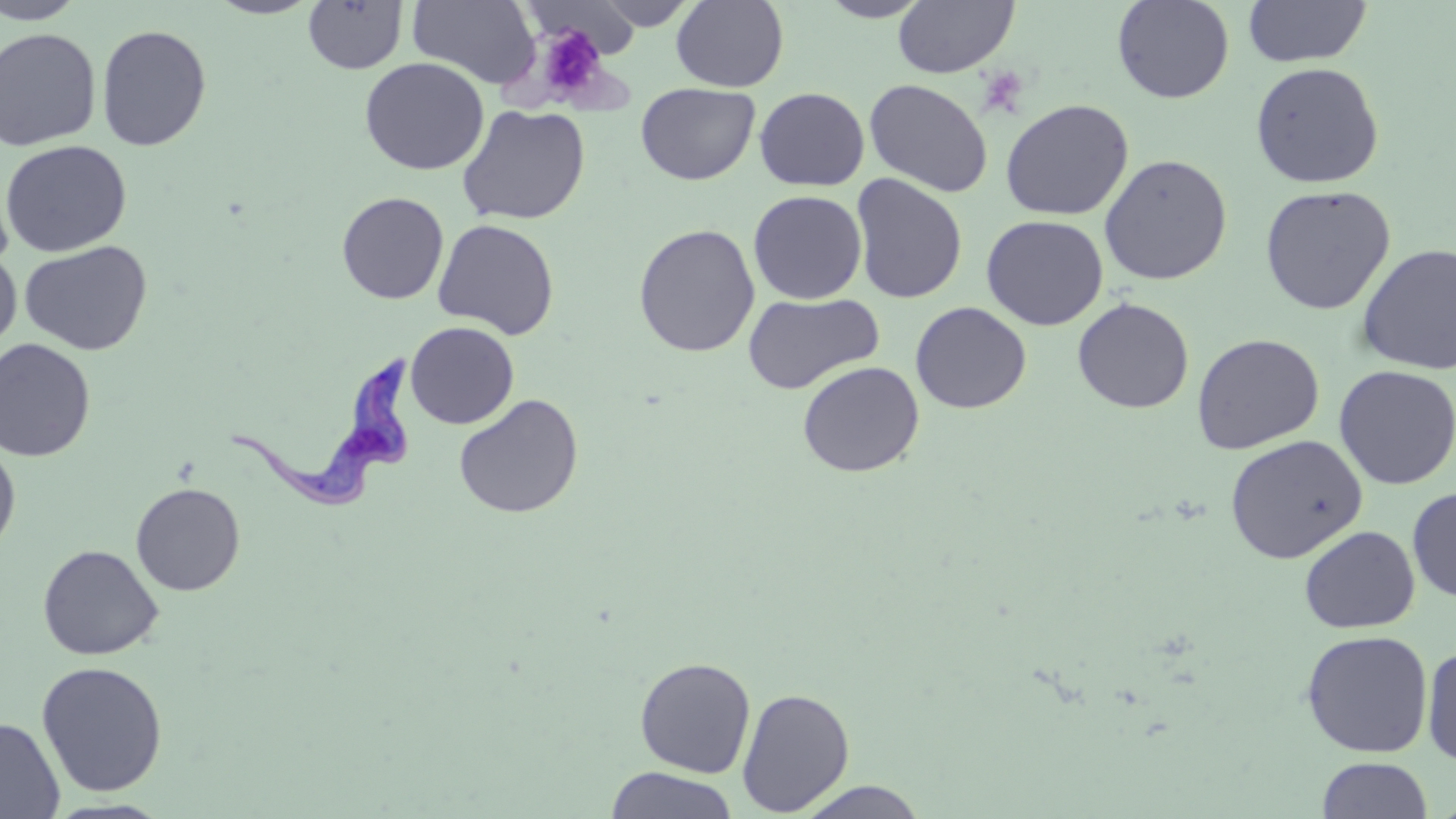
slide-level diagnosis = Trypanosoma brucei
preparation = thin blood film
stain = May-Grünwald-Giemsa
platelet locations = approximate bounding boxes as (x1,y1)-(x2,y2) corner pairs in pixels: (531,25)-(611,105), (977,66)-(1031,117)
magnification = 1000x
image size = 1456×819 pixels
Trypanosoma brucei locations = approximate bounding boxes as (x1,y1)-(x2,y2) corner pairs in pixels: (229,349)-(420,515)
field of view = one of a larger specimen
modality = light microscopy
uninfected red blood cell locations = approximate bounding boxes as (x1,y1)-(x2,y2) corner pairs in pixels: (0,0)-(88,24), (205,0)-(323,19), (407,0)-(539,89), (593,0)-(700,30), (815,0)-(935,22), (892,0)-(1019,78), (1111,0)-(1235,104), (1242,0)-(1373,68), (303,1)-(408,74), (526,1)-(642,58), (670,1)-(789,92), (96,24)-(212,151), (0,27)-(102,151), (359,57)-(490,175), (1249,61)-(1385,189), (864,78)-(994,197), (635,82)-(760,185), (754,87)-(870,191), (1000,98)-(1134,221), (456,103)-(591,225), (0,139)-(132,257), (1098,153)-(1233,285), (850,173)-(968,304), (1259,184)-(1396,315), (748,189)-(867,304), (336,191)-(449,304), (981,214)-(1108,331), (432,218)-(560,339), (633,223)-(760,357), (19,240)-(153,356), (1355,242)-(1456,376), (0,246)-(22,351), (742,291)-(884,396), (1072,297)-(1194,413), (910,301)-(1031,414), (405,321)-(519,429), (1191,332)-(1325,454), (0,338)-(96,462), (797,360)-(925,477), (1333,365)-(1455,490), (453,393)-(583,519), (1224,434)-(1367,564), (0,439)-(21,557), (130,482)-(246,596), (1407,486)-(1455,602), (1299,525)-(1420,634), (37,543)-(164,660), (1300,630)-(1434,758), (1422,644)-(1456,767), (634,656)-(756,778), (35,660)-(168,797), (736,687)-(855,816), (0,717)-(65,819), (1316,757)-(1432,818), (604,767)-(740,818), (794,780)-(930,819)